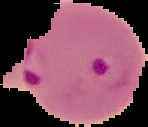

Image is 148×127 pixels. Cell region segmented out of the field of view; the surrounding area is masked to black. Result: malaria parasites detected. From a thin blood smear.